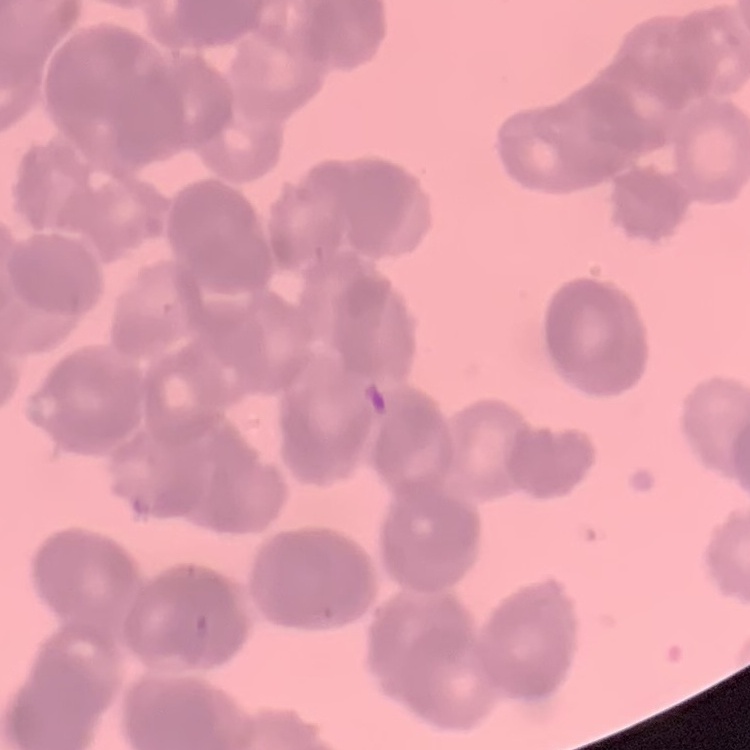
red blood cell morphology = rouleaux formation
image type = square crop of a larger photomicrograph
stain = Field's or Giemsa
preparation = thin blood smear